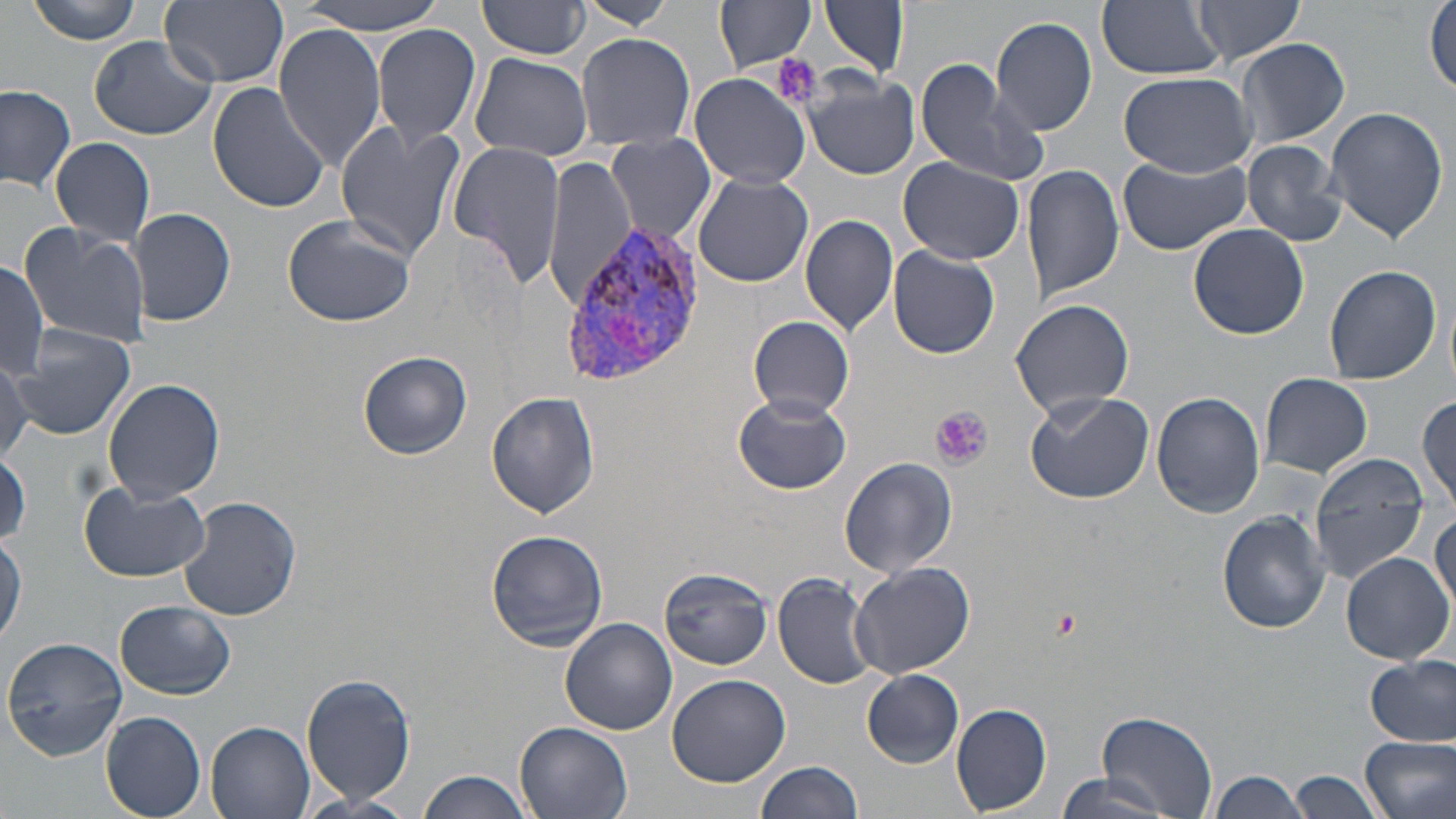

Summary:
  - Coordinate format: approximate bounding boxes as (x1,y1)-(x2,y2) corner pairs in pixels
  - Uninfected red blood cell locations: (26,0)-(147,45), (159,0)-(288,88), (296,0)-(451,34), (479,0)-(593,59), (583,0)-(673,30), (1097,1)-(1225,79), (821,2)-(910,79), (1191,2)-(1305,65), (717,3)-(816,73), (1425,3)-(1455,97), (989,15)-(1100,137), (273,24)-(389,171), (371,24)-(481,150), (575,31)-(696,153), (87,35)-(217,140), (1236,37)-(1351,150), (469,52)-(595,162), (917,62)-(1050,187), (805,70)-(920,180), (1119,71)-(1255,177), (689,72)-(811,189), (208,81)-(331,214), (0,84)-(76,192), (1323,106)-(1450,246), (334,119)-(463,265), (607,132)-(716,244), (51,136)-(154,248), (1241,140)-(1346,246), (448,141)-(567,290), (543,153)-(635,311), (1118,155)-(1249,257), (898,157)-(1024,265), (1022,164)-(1123,302), (691,174)-(815,289), (130,206)-(236,328), (798,212)-(899,337), (282,214)-(416,328), (18,223)-(150,351), (1188,223)-(1309,340), (889,246)-(1000,359), (0,262)-(51,379), (1323,264)-(1442,386), (1011,298)-(1134,417), (748,315)-(855,419), (10,325)-(136,441), (357,350)-(472,460), (0,353)-(30,461), (1260,372)-(1374,478), (102,378)-(224,504), (1024,390)-(1154,503), (486,391)-(600,518), (1152,392)-(1265,519), (733,394)-(851,495), (1416,394)-(1455,517), (0,450)-(31,548), (1310,453)-(1429,580), (840,457)-(957,577), (79,482)-(210,583), (179,495)-(301,621), (1218,510)-(1331,634), (1430,512)-(1455,615), (1,529)-(25,648), (485,530)-(609,651), (1340,551)-(1453,665), (848,562)-(976,679), (659,567)-(773,669), (773,571)-(879,689), (116,600)-(235,699), (560,618)-(677,735), (1,636)-(127,759), (1365,655)-(1455,747), (862,670)-(964,766), (301,672)-(417,806), (665,675)-(790,788), (951,703)-(1052,815), (99,711)-(206,818), (1098,711)-(1218,817), (205,719)-(316,819), (515,721)-(633,819), (1360,733)-(1456,819), (755,759)-(864,818), (419,769)-(533,819), (1206,769)-(1306,819), (1290,769)-(1385,819), (1050,774)-(1180,819), (297,792)-(419,819)
  - Plasmodium vivax-infected red blood cell locations: (561,223)-(702,386)
  - Platelet locations: (775,53)-(821,108), (933,407)-(991,469), (1053,606)-(1080,638)
  - Slide-level diagnosis: Plasmodium vivax
  - Field of view: one of a larger specimen
  - Magnification: 1000x
  - Modality: light microscopy
  - Stain: May-Grünwald-Giemsa
  - Preparation: thin blood smear
  - Image size: 1456×819 pixels